Outline each blood parasite and name the species.
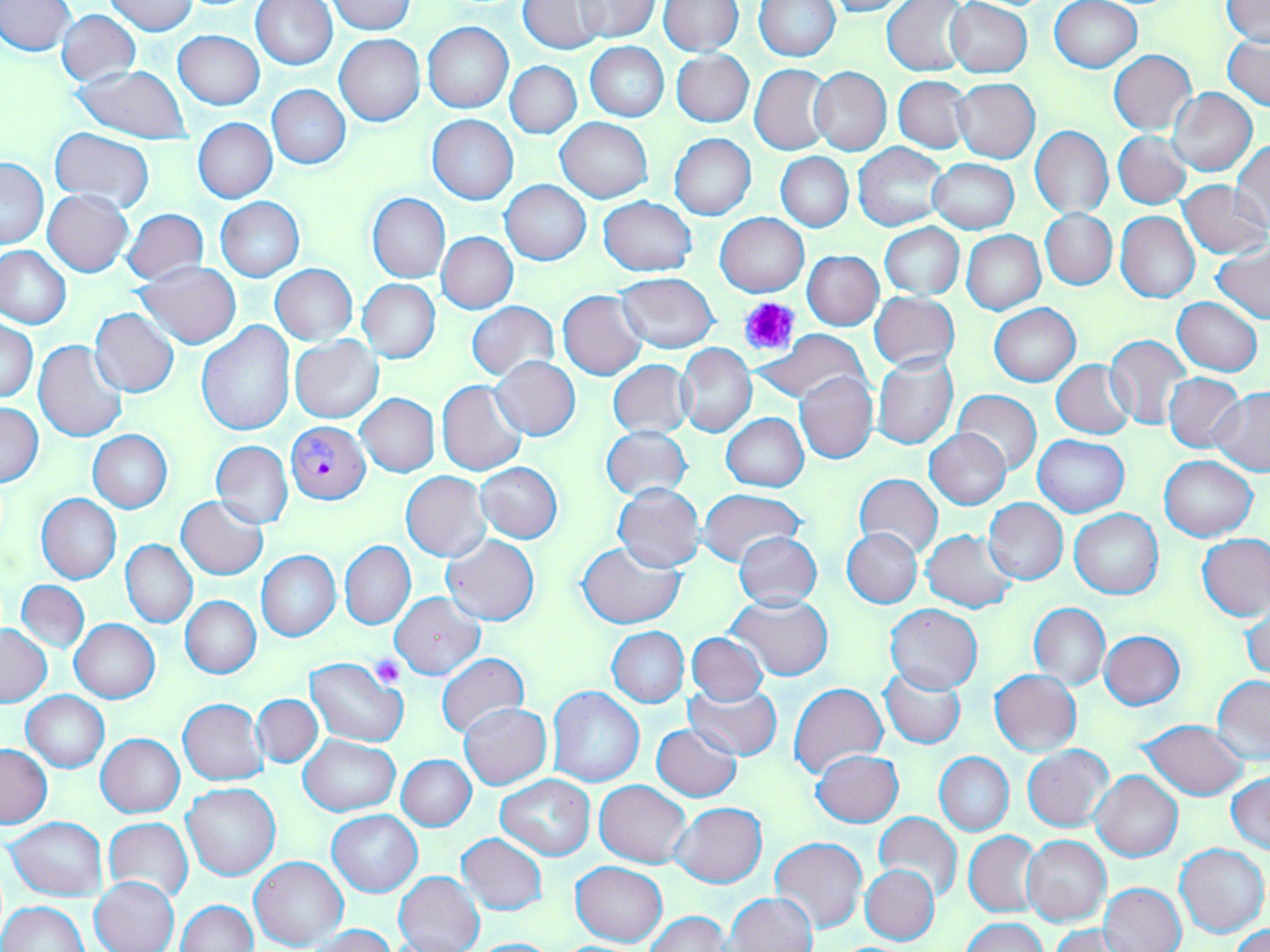
Approximate bounding boxes as (x1, y1, x2, y2) in pixels.
Plasmodium falciparum-infected red blood cells: (286, 420, 370, 504).
No Plasmodium ovale, Plasmodium malariae, Plasmodium vivax, Babesia divergens, or Trypanosoma brucei observed.

Summary:
  - Platelet locations: (741, 297, 802, 355), (371, 655, 405, 686)
  - Uninfected red blood cell locations: (519, 0, 605, 53), (575, 0, 659, 40), (818, 0, 912, 16), (945, 0, 1032, 78), (1050, 0, 1143, 73), (1222, 0, 1269, 46), (1, 1, 75, 55), (106, 1, 200, 34), (251, 1, 337, 71), (325, 1, 414, 34), (658, 1, 742, 55), (754, 1, 839, 61), (883, 1, 972, 75), (58, 10, 140, 86), (424, 22, 513, 114), (173, 30, 264, 109), (335, 34, 425, 126), (1224, 34, 1270, 110), (586, 42, 669, 122), (1108, 51, 1196, 134), (671, 52, 753, 126), (506, 61, 581, 138), (750, 64, 832, 154), (73, 65, 192, 144), (809, 67, 892, 155), (893, 76, 971, 153), (952, 78, 1039, 164), (266, 84, 350, 169), (1168, 87, 1256, 177), (428, 115, 518, 205), (193, 118, 276, 203), (556, 118, 652, 202), (1029, 125, 1113, 218), (50, 127, 155, 212), (1114, 131, 1191, 210), (670, 133, 756, 219), (1232, 141, 1270, 230), (852, 144, 948, 230), (776, 152, 853, 230), (928, 158, 1019, 233), (1, 159, 48, 248), (500, 181, 590, 265), (1178, 181, 1270, 258), (43, 190, 133, 276), (367, 193, 450, 283), (599, 196, 697, 277), (216, 197, 304, 281), (1040, 209, 1117, 290), (123, 210, 207, 287), (1115, 212, 1200, 303), (716, 213, 808, 296), (880, 223, 963, 298), (962, 230, 1045, 314), (437, 232, 518, 313), (0, 246, 72, 330), (1212, 246, 1270, 323), (803, 251, 884, 330), (134, 263, 241, 348), (271, 266, 357, 345), (615, 273, 719, 353), (360, 279, 440, 362), (558, 290, 647, 380), (870, 292, 960, 371), (1173, 298, 1262, 376), (467, 301, 558, 381), (990, 304, 1081, 386), (90, 308, 180, 398), (1, 320, 38, 402), (196, 321, 296, 435), (757, 329, 872, 405), (1105, 334, 1191, 429), (290, 337, 383, 422), (34, 340, 129, 443), (675, 343, 757, 437), (872, 354, 958, 449), (490, 357, 580, 440), (608, 360, 693, 438), (1052, 360, 1135, 439), (795, 372, 878, 464), (1164, 373, 1246, 453), (437, 380, 527, 475), (1210, 388, 1270, 476), (952, 390, 1040, 476), (356, 394, 439, 477), (1, 403, 43, 487), (722, 413, 809, 491), (600, 425, 692, 501), (925, 428, 1012, 510), (89, 431, 173, 512), (1034, 435, 1129, 516), (210, 440, 292, 529), (1160, 456, 1257, 541), (477, 463, 563, 542), (401, 471, 492, 562), (854, 472, 942, 559), (612, 483, 706, 573), (698, 488, 807, 564), (37, 494, 121, 583), (176, 496, 269, 580), (984, 499, 1067, 584), (1069, 508, 1163, 598), (843, 528, 922, 607), (920, 529, 1018, 612), (733, 531, 822, 609), (1197, 533, 1269, 620), (441, 535, 539, 625), (121, 540, 196, 627), (340, 541, 415, 629), (577, 541, 684, 629), (256, 551, 340, 641), (18, 580, 89, 652), (390, 592, 485, 680), (726, 594, 833, 679), (180, 596, 260, 679), (1241, 600, 1270, 682), (1027, 603, 1110, 689), (884, 604, 982, 693), (71, 619, 159, 703), (0, 624, 51, 707), (607, 627, 689, 706), (1100, 630, 1186, 709), (686, 632, 768, 705), (366, 652, 407, 689), (437, 654, 528, 739), (306, 656, 410, 748), (880, 667, 965, 749), (990, 670, 1081, 757), (1212, 676, 1270, 764), (684, 683, 781, 760), (789, 683, 887, 778), (547, 686, 643, 787), (23, 691, 108, 772), (252, 694, 322, 767), (178, 698, 267, 785), (459, 703, 551, 788), (1137, 719, 1252, 799), (652, 723, 742, 801), (96, 733, 185, 818), (300, 735, 399, 816), (0, 743, 52, 827), (1023, 745, 1113, 831), (811, 750, 904, 827), (934, 751, 1014, 835), (397, 755, 476, 830), (1091, 770, 1183, 862), (1227, 773, 1270, 854), (497, 775, 594, 859), (594, 780, 692, 867), (182, 782, 280, 880), (672, 802, 766, 888), (328, 809, 423, 896), (874, 812, 962, 902), (7, 817, 107, 901), (103, 818, 193, 903), (964, 831, 1040, 917), (457, 833, 547, 916), (1022, 836, 1111, 926), (771, 837, 866, 934), (1175, 843, 1269, 937), (250, 856, 348, 950), (1101, 860, 1262, 945), (571, 861, 667, 946), (860, 863, 940, 945), (395, 871, 484, 952), (90, 876, 179, 951), (1100, 882, 1185, 952), (725, 892, 818, 952), (0, 900, 87, 952), (177, 900, 257, 952), (645, 912, 729, 952), (961, 918, 1047, 952), (1228, 924, 1270, 952), (1047, 925, 1133, 951), (308, 926, 397, 952), (466, 938, 564, 951)
  - Slide-level diagnosis: Plasmodium falciparum
  - Modality: light microscopy
  - Stain: May-Grünwald-Giemsa
  - Preparation: thin blood film
  - Magnification: 1000x
  - Image size: 1270×952 pixels
  - Field of view: single